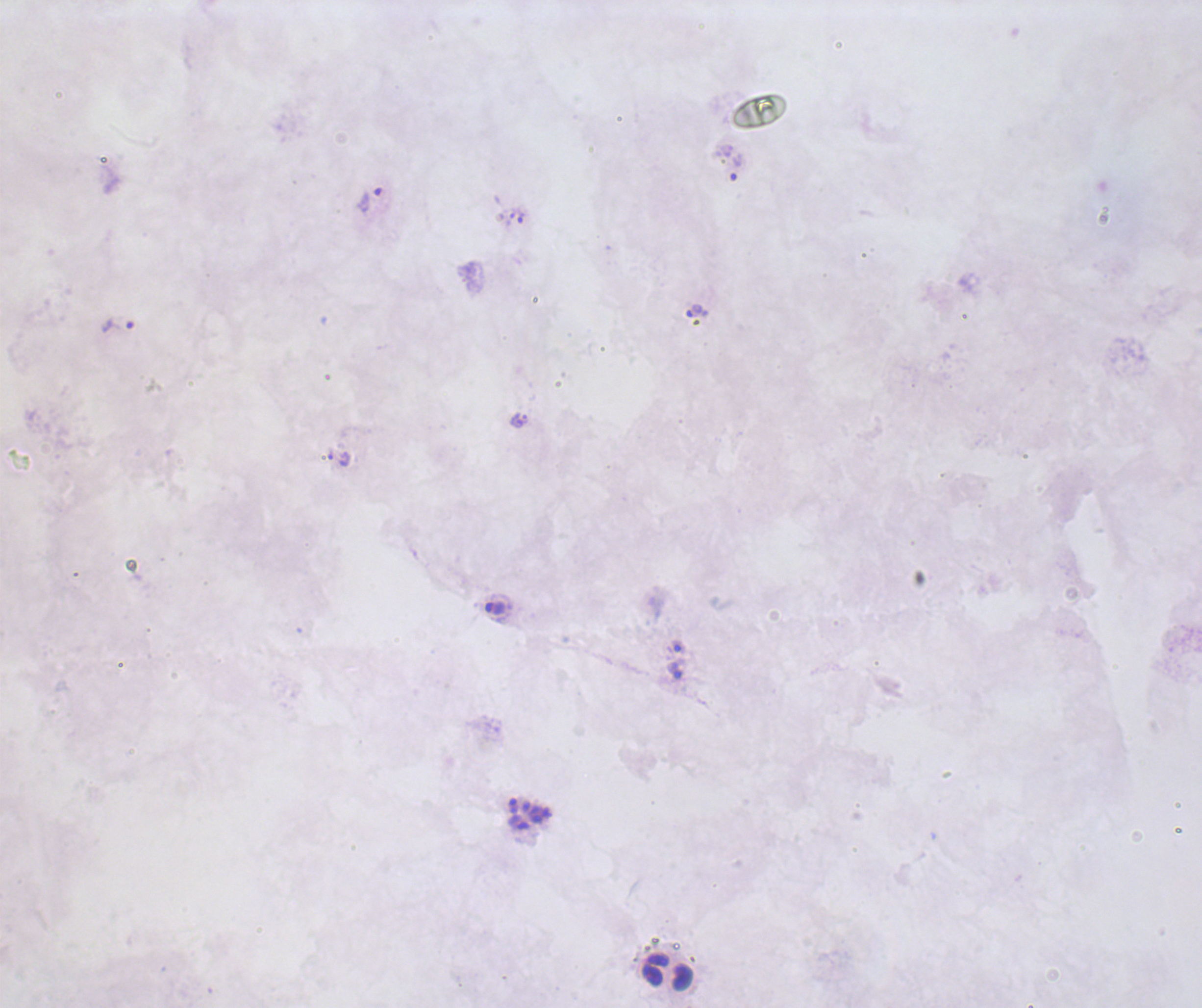
coordinate format = approximate centers as [x, y] in pixels
leukocyte locations = [667, 972]
trophozoite locations = [736, 166], [370, 201], [521, 217], [697, 310], [116, 324], [519, 420], [339, 458], [496, 609], [678, 646], [675, 671]
schizont locations = [529, 813]
life-cycle stages observed = trophozoite, schizont
coloration quality = bad
context = previously used in a real diagnosis
magnification = 100x
preparation = thick smear of blood
field of view = single
result = Plasmodium parasites identified
stain = Romanowsky
image size = 1202×1008 pixels
background quality = poor